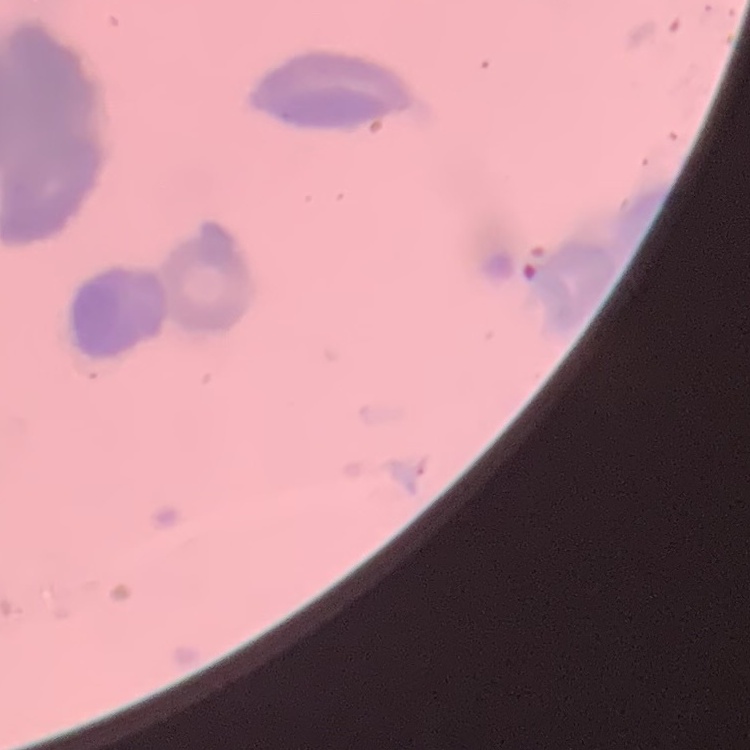
Summary:
  - Erythrocyte morphology: rouleaux formation
  - Stain: Field's or Giemsa
  - Image type: one tile cut from a larger photomicrograph
  - Preparation: thin blood film